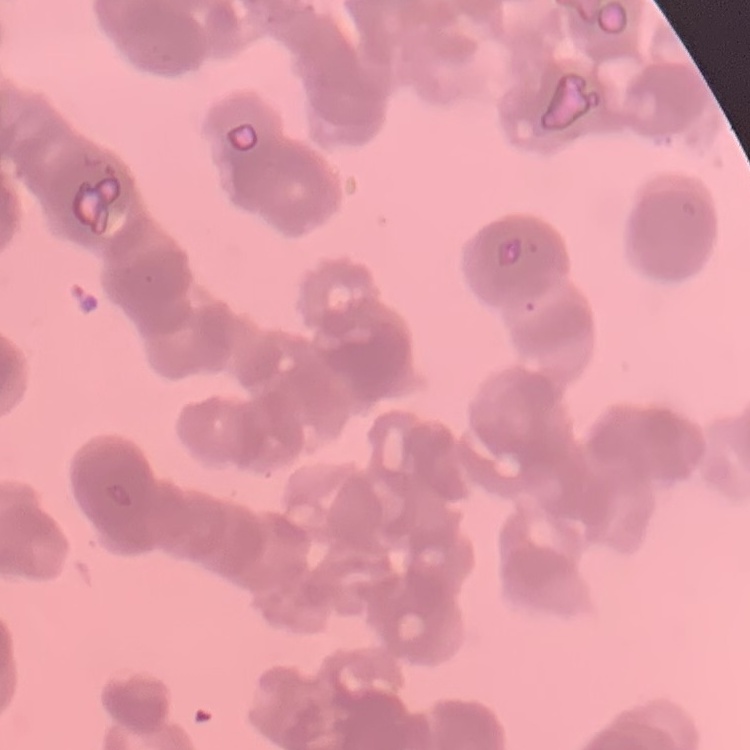
The erythrocytes show rouleaux formation. Stained with either Field's or Giemsa. One tile cut from a larger photomicrograph. Thin blood film.